Report the malaria status of this cell.
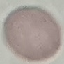

Uninfected.

Summary:
  - Image type: automatically extracted cell patch, resized to 64 × 64 pixels
  - Stain: Giemsa
  - Preparation: thin blood smear
  - Capture: smartphone camera at the microscope eyepiece